Report the malaria status of this cell.
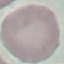

It is uninfected.

Acquired by smartphone through the microscope eyepiece. Cell patch, automatically extracted from a larger field of view and resized to 64 × 64 pixels. Thin smear of blood. Giemsa stain.